Comment on the morphology of the erythrocytes.
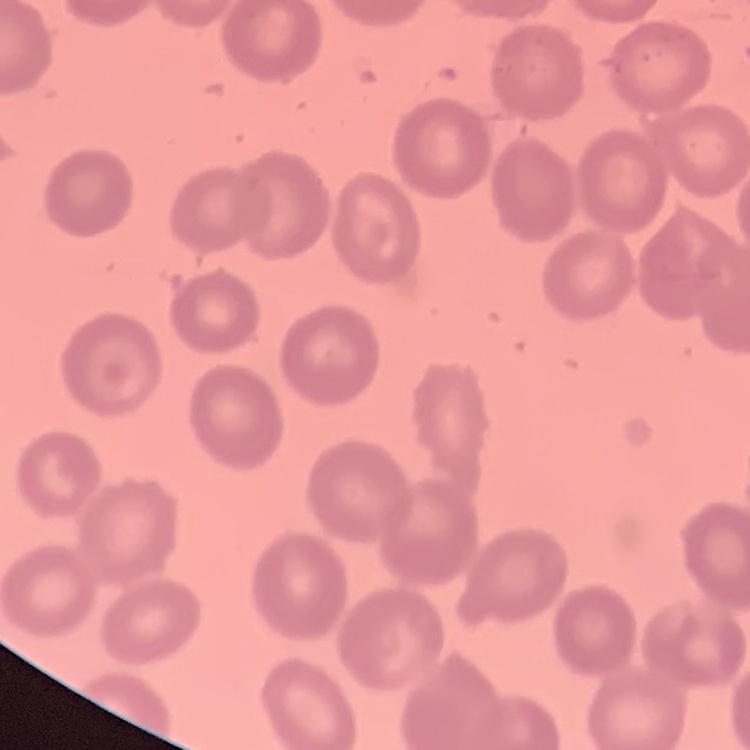
No rouleaux formation.

Summary:
  - Stain: Field's or Giemsa
  - Preparation: thin blood film
  - Image type: one tile cut from a larger photomicrograph